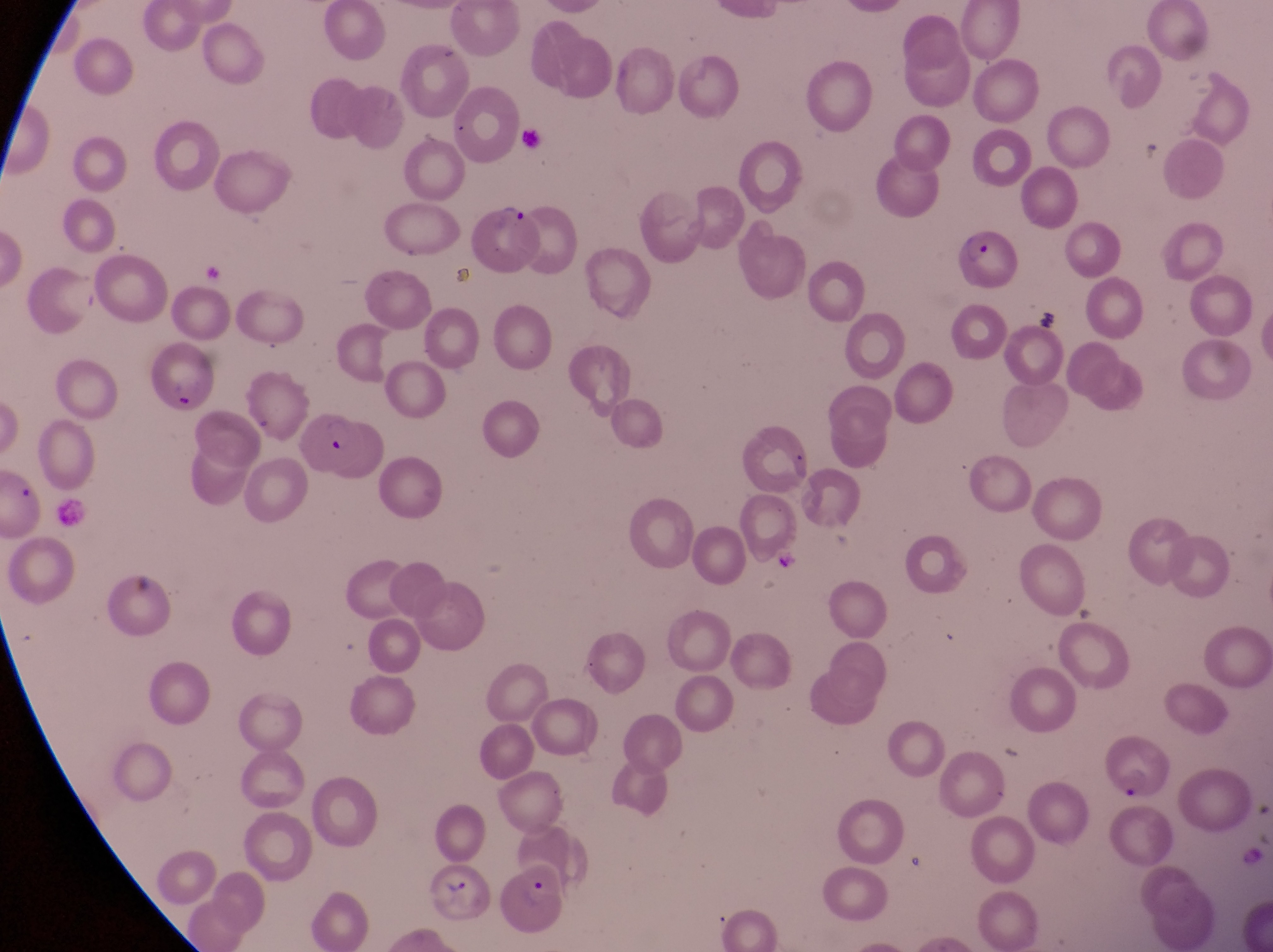
Approximate bounding boxes as {left, top, right, bottom} in pixels.
Summary:
  - Parasitised red blood cell locations: {477, 204, 535, 272}, {958, 227, 1021, 294}, {150, 340, 213, 415}, {1103, 735, 1177, 805}, {422, 864, 492, 926}, {497, 867, 571, 939}
  - Artifact (platelet-like body, stain precipitate, or debris) locations: {514, 125, 541, 147}, {1031, 300, 1070, 335}
  - Trophozoite locations: {1133, 137, 1172, 177}
  - Country: Uganda
  - Magnification: 1000x
  - Capture: smartphone photograph through the eyepiece of an Olympus CX-23 microscope
  - Field of view: single
  - Preparation: thin blood film
  - Image size: 1273×952 pixels